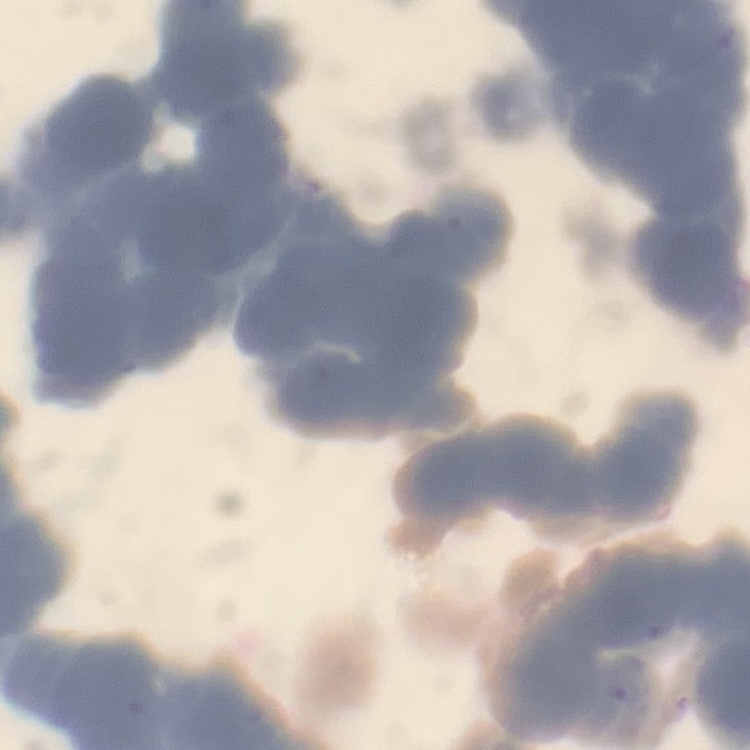 The erythrocytes exhibit rouleaux formation. Square crop of a larger photomicrograph. Thin blood smear. Stained with either Field's or Giemsa.